Assess this cell for malaria.
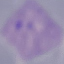
Parasitized.

{
  "stain": "Giemsa",
  "preparation": "thin blood smear",
  "capture": "smartphone through the microscope eyepiece",
  "image_type": "automatically extracted cell patch, resized to 64 × 64 pixels"
}